Report the malaria status of this cell.
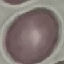
It is uninfected.

Acquired by smartphone through the microscope eyepiece. Cell patch, automatically extracted from a larger field of view and resized to 64 × 64 pixels. Thin blood film. Giemsa stain.